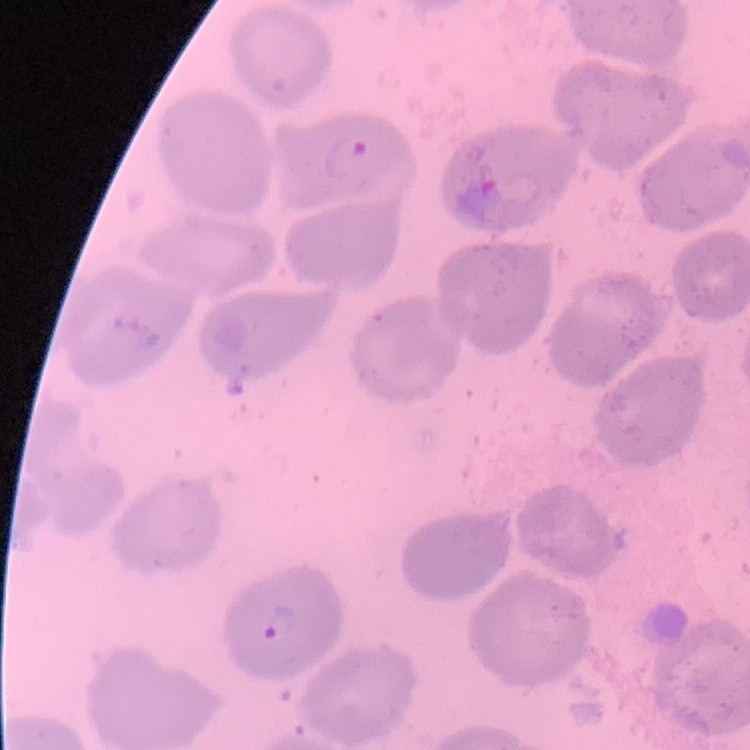

red blood cell morphology = no rouleaux formation
image type = square crop of a larger photomicrograph
preparation = thin blood film
stain = Field's or Giemsa